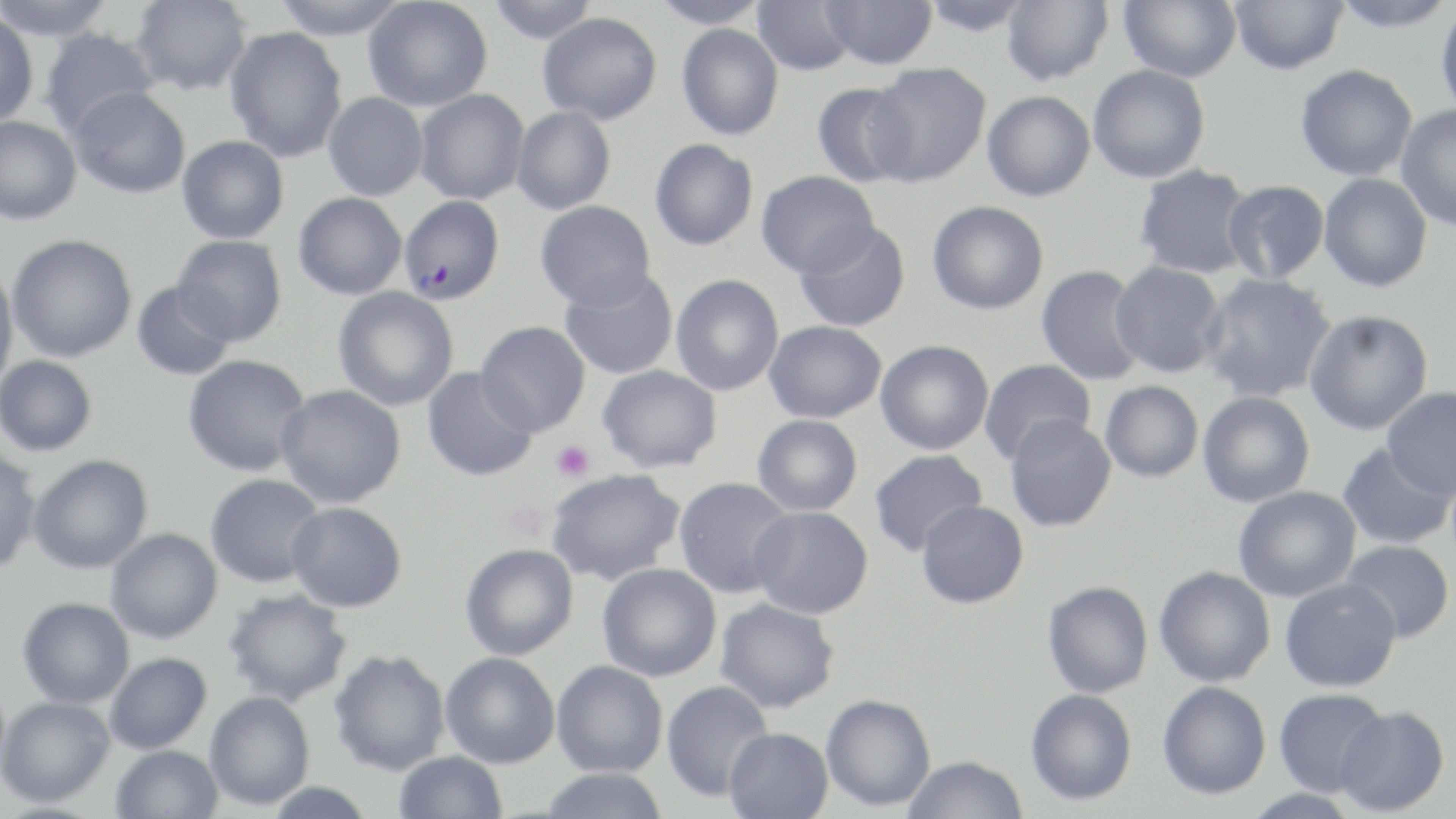
slide-level diagnosis = Plasmodium falciparum
stain = May-Grünwald-Giemsa
preparation = thin blood smear
field of view = single
platelet locations = approximate bounding boxes as (x1,y1)-(x2,y2) corner pairs in pixels: (551,441)-(594,482), (502,501)-(551,544)
modality = light microscopy
magnification = 1000x
Plasmodium falciparum-infected red blood cell locations = approximate bounding boxes as (x1,y1)-(x2,y2) corner pairs in pixels: (399,194)-(505,304)
uninfected red blood cell locations = approximate bounding boxes as (x1,y1)-(x2,y2) corner pairs in pixels: (1,0)-(118,42), (130,0)-(252,95), (272,0)-(411,40), (363,0)-(492,112), (488,0)-(598,44), (650,0)-(770,29), (752,0)-(857,76), (820,0)-(938,70), (919,0)-(1034,37), (1001,0)-(1113,86), (1118,0)-(1241,82), (1229,0)-(1347,74), (1329,0)-(1456,33), (1435,3)-(1456,120), (0,11)-(39,126), (537,12)-(662,125), (676,23)-(784,140), (224,27)-(348,163), (38,28)-(162,137), (866,62)-(991,187), (1295,64)-(1418,181), (1088,65)-(1210,183), (810,82)-(915,187), (69,86)-(191,199), (414,89)-(530,205), (982,90)-(1096,201), (323,92)-(428,200), (1396,104)-(1456,233), (511,106)-(616,215), (0,115)-(82,226), (177,136)-(289,244), (649,138)-(758,251), (1134,164)-(1255,279), (755,170)-(880,278), (1318,173)-(1432,292), (1223,180)-(1330,285), (294,192)-(407,300), (534,200)-(656,310), (927,200)-(1048,314), (794,221)-(911,332), (6,234)-(137,362), (172,234)-(287,345), (1110,260)-(1227,378), (0,264)-(19,395), (1035,264)-(1148,386), (559,268)-(679,379), (1199,273)-(1337,403), (671,274)-(784,396), (131,280)-(236,381), (332,286)-(459,411), (1304,309)-(1434,436), (764,320)-(887,423), (475,321)-(591,437), (875,340)-(994,455), (183,354)-(312,477), (0,355)-(97,457), (979,358)-(1096,465), (597,364)-(724,473), (421,367)-(537,482), (1100,380)-(1203,482), (276,384)-(405,508), (1381,387)-(1456,499), (1197,392)-(1315,508), (752,414)-(863,516), (1004,414)-(1117,532), (1337,442)-(1454,550), (0,448)-(42,575), (869,448)-(987,557), (28,454)-(153,574), (545,468)-(685,586), (205,473)-(325,588), (674,477)-(797,598), (1232,486)-(1362,602), (917,500)-(1029,608), (286,501)-(407,612), (749,506)-(874,619), (106,528)-(222,643), (1340,539)-(1454,642), (460,544)-(579,661), (597,563)-(722,681), (1154,566)-(1275,687), (1279,579)-(1401,693), (1042,580)-(1153,698), (221,587)-(352,707), (17,596)-(134,709), (714,597)-(839,713), (329,649)-(449,776), (440,652)-(560,768), (105,653)-(212,754), (551,660)-(668,777), (661,680)-(774,802), (1157,681)-(1271,799), (1025,688)-(1137,805), (1273,688)-(1390,797), (205,691)-(315,810), (820,694)-(935,811), (0,696)-(115,808), (1335,705)-(1450,816), (724,728)-(834,819), (112,745)-(224,819), (394,751)-(507,819), (902,756)-(1028,819), (539,767)-(670,819), (1242,788)-(1359,818)
image size = 1456×819 pixels